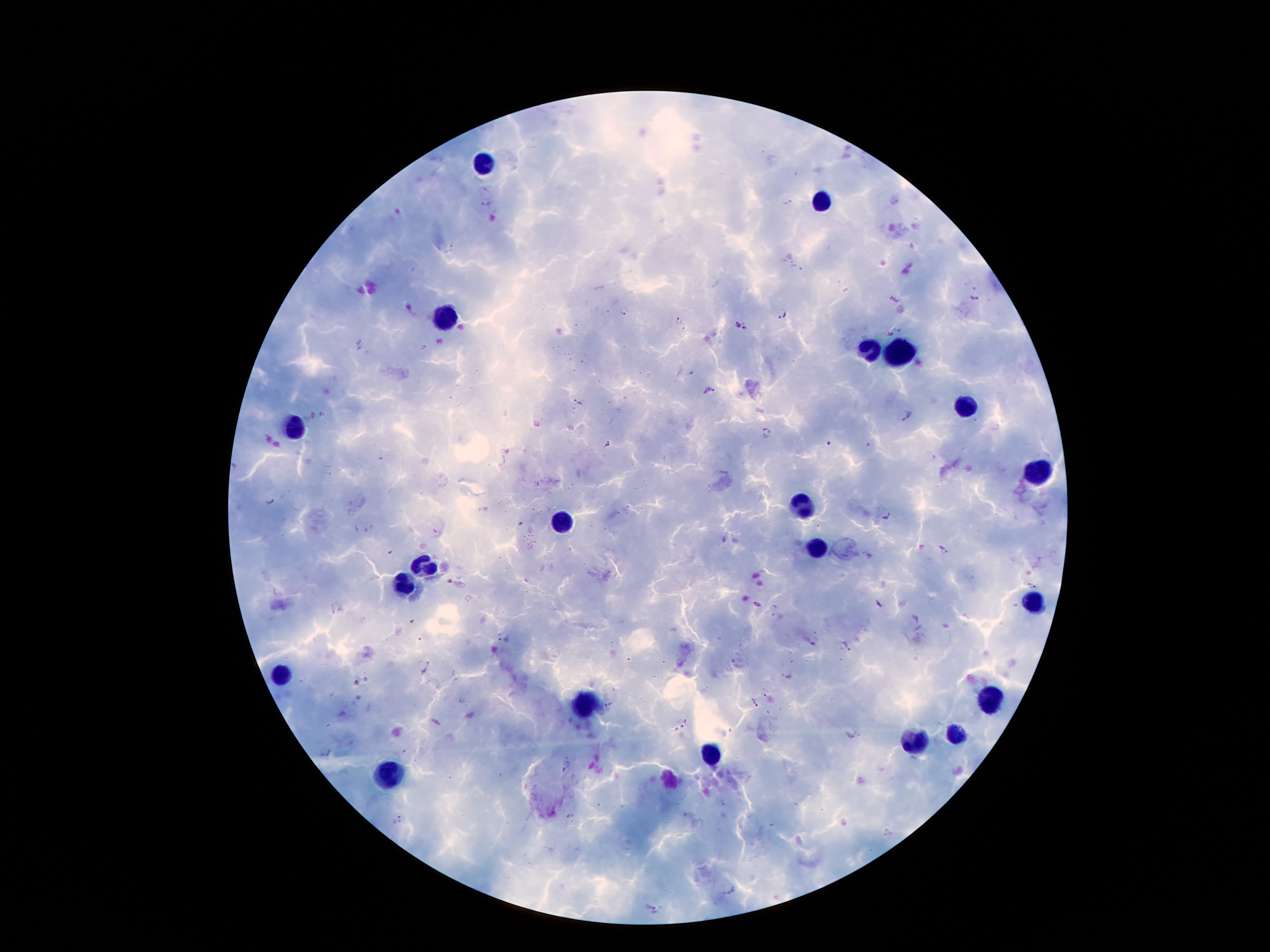 Approximate object centers, in pixels from the top-left corner. Malaria parasite locations: (x=487, y=199), (x=787, y=203), (x=450, y=249), (x=975, y=298), (x=624, y=309), (x=784, y=313), (x=678, y=323), (x=736, y=323), (x=746, y=327), (x=898, y=328), (x=362, y=345), (x=690, y=372), (x=709, y=391), (x=578, y=402), (x=908, y=416), (x=767, y=433), (x=606, y=443), (x=828, y=445), (x=932, y=458), (x=270, y=500), (x=887, y=515), (x=944, y=546), (x=1033, y=586), (x=757, y=603), (x=878, y=604), (x=333, y=610), (x=778, y=617), (x=503, y=637), (x=424, y=666), (x=766, y=691), (x=463, y=700), (x=754, y=704), (x=608, y=705), (x=437, y=722), (x=686, y=723), (x=850, y=736), (x=325, y=752), (x=723, y=803), (x=570, y=816), (x=399, y=819), (x=656, y=910). Leukocyte locations: (x=485, y=161), (x=821, y=200), (x=445, y=317), (x=868, y=347), (x=892, y=352), (x=968, y=405), (x=295, y=428), (x=1038, y=468), (x=805, y=502), (x=563, y=522), (x=818, y=549), (x=424, y=567), (x=404, y=583), (x=1033, y=601), (x=282, y=675), (x=993, y=696), (x=584, y=702), (x=957, y=735), (x=912, y=743), (x=710, y=754), (x=387, y=777). 100x magnification. Giemsa stain. Thick blood film. One field from this slide. Image is 1270×952 pixels. Patient malaria status: positive for Plasmodium falciparum. Smartphone photograph taken through the microscope eyepiece.